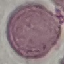
{
  "result": "no malaria parasites detected",
  "capture": "smartphone camera at the microscope eyepiece",
  "image_type": "cell patch, automatically extracted from a larger field of view and resized to 64 × 64 pixels",
  "stain": "Giemsa",
  "preparation": "thin blood smear"
}